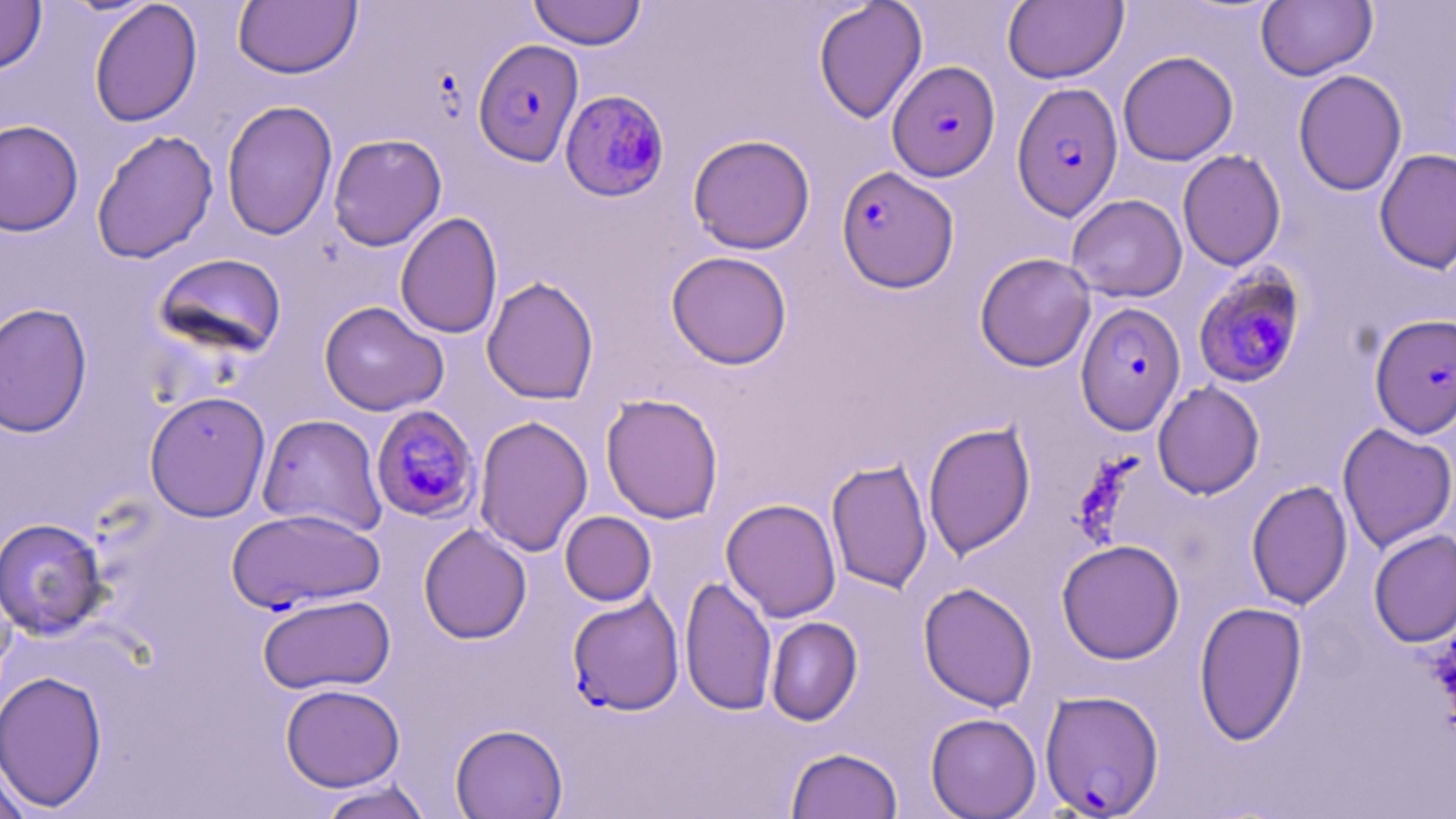

Approximate bounding boxes as [x1, y1, x2, y2] in pixels. Plasmodium falciparum-infected red blood cell locations: [473, 39, 584, 167], [887, 61, 1000, 182], [1011, 82, 1124, 221], [559, 89, 671, 202], [835, 165, 959, 293], [1192, 265, 1307, 389], [1075, 302, 1186, 435], [1369, 313, 1456, 439], [370, 405, 481, 523], [228, 507, 385, 613], [567, 593, 684, 715], [1039, 690, 1165, 817]. Uninfected red blood cell locations: [0, 0, 47, 74], [89, 0, 203, 127], [527, 0, 647, 50], [233, 1, 362, 79], [813, 1, 928, 124], [1003, 1, 1127, 84], [1256, 1, 1377, 80], [1118, 50, 1238, 166], [1292, 70, 1407, 196], [221, 100, 338, 240], [0, 119, 84, 236], [91, 129, 219, 264], [327, 133, 447, 251], [687, 134, 816, 254], [1374, 148, 1456, 275], [1177, 149, 1286, 271], [1066, 194, 1187, 302], [395, 211, 502, 340], [666, 251, 793, 370], [154, 252, 288, 359], [974, 252, 1096, 372], [481, 276, 599, 404], [319, 301, 448, 415], [0, 302, 92, 437], [1152, 380, 1265, 500], [144, 390, 272, 522], [600, 393, 724, 524], [257, 414, 388, 537], [474, 414, 594, 557], [923, 421, 1036, 558], [1337, 422, 1456, 553], [826, 457, 933, 593], [1246, 479, 1352, 610], [721, 498, 842, 622], [560, 511, 657, 606], [0, 517, 110, 640], [418, 524, 532, 644], [1368, 528, 1456, 648], [1057, 539, 1185, 664], [679, 575, 777, 716], [918, 582, 1038, 712], [257, 593, 396, 694], [1193, 600, 1308, 745], [765, 616, 863, 726], [0, 670, 108, 811], [280, 683, 405, 791], [925, 712, 1042, 818], [450, 723, 568, 819], [785, 746, 903, 819], [0, 756, 32, 819], [316, 780, 435, 819]. Slide-level diagnosis: Plasmodium falciparum. Single field of view. Optical microscopy. Image is 1456×819 pixels. Captured at 1000x magnification. May-Grünwald-Giemsa-stained preparation. Thin blood film.